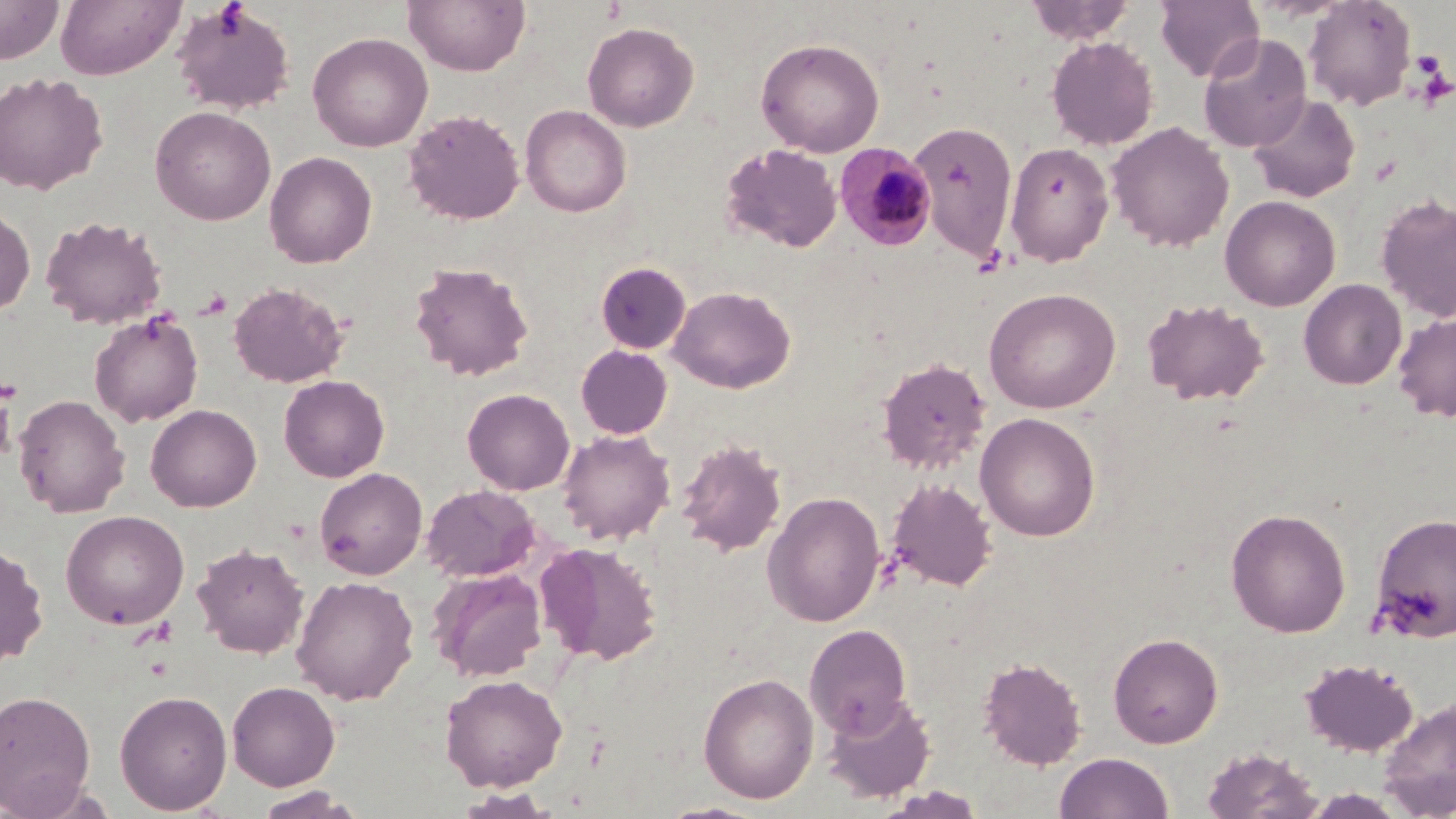
slide-level diagnosis = Plasmodium malariae
stain = May-Grünwald-Giemsa
image size = 1456×819 pixels
preparation = thin blood film
Plasmodium malariae-infected red blood cell locations = approximate bounding boxes as [x1, y1, x2, y2] in pixels: [834, 143, 937, 251]
uninfected red blood cell locations = approximate bounding boxes as [x1, y1, x2, y2] in pixels: [0, 0, 63, 63], [55, 0, 184, 80], [403, 0, 530, 76], [1026, 0, 1137, 44], [1155, 0, 1263, 82], [1302, 0, 1416, 111], [171, 3, 296, 115], [582, 22, 699, 132], [308, 32, 433, 152], [1198, 32, 1312, 152], [1046, 36, 1159, 151], [755, 37, 885, 157], [0, 71, 108, 195], [1247, 93, 1361, 203], [520, 105, 631, 217], [150, 106, 276, 225], [403, 108, 525, 225], [909, 121, 1018, 262], [1107, 121, 1234, 252], [1004, 141, 1114, 266], [721, 143, 842, 253], [264, 151, 377, 268], [1376, 193, 1456, 322], [1220, 195, 1341, 311], [0, 207, 36, 316], [40, 215, 167, 330], [409, 260, 534, 381], [595, 261, 691, 354], [1299, 279, 1406, 390], [228, 281, 349, 388], [668, 285, 796, 393], [983, 287, 1121, 414], [1142, 297, 1270, 406], [89, 311, 203, 427], [1393, 312, 1456, 423], [576, 345, 672, 438], [876, 357, 990, 473], [278, 375, 390, 482], [462, 388, 575, 495], [12, 394, 130, 517], [146, 404, 261, 512], [975, 412, 1100, 542], [557, 428, 676, 545], [676, 437, 787, 557], [314, 467, 427, 580], [886, 477, 997, 592], [420, 483, 541, 583], [762, 491, 886, 627], [1225, 507, 1351, 637], [60, 509, 189, 629], [1371, 512, 1456, 641], [536, 541, 663, 666], [192, 542, 309, 658], [0, 543, 48, 667], [428, 567, 547, 681], [291, 575, 419, 705], [804, 623, 912, 736], [1108, 631, 1223, 748], [977, 656, 1087, 770], [1299, 657, 1419, 757], [698, 672, 818, 804], [439, 674, 567, 792], [227, 680, 340, 790], [114, 689, 232, 815], [0, 690, 96, 815], [821, 692, 936, 803], [1376, 695, 1456, 818], [1200, 746, 1324, 819], [1054, 752, 1173, 819], [252, 786, 367, 819]
field of view = one of a larger specimen
platelet locations = approximate bounding boxes as [x1, y1, x2, y2] in pixels: [1412, 51, 1445, 77], [1413, 59, 1453, 106]
magnification = 1000x
modality = light microscopy